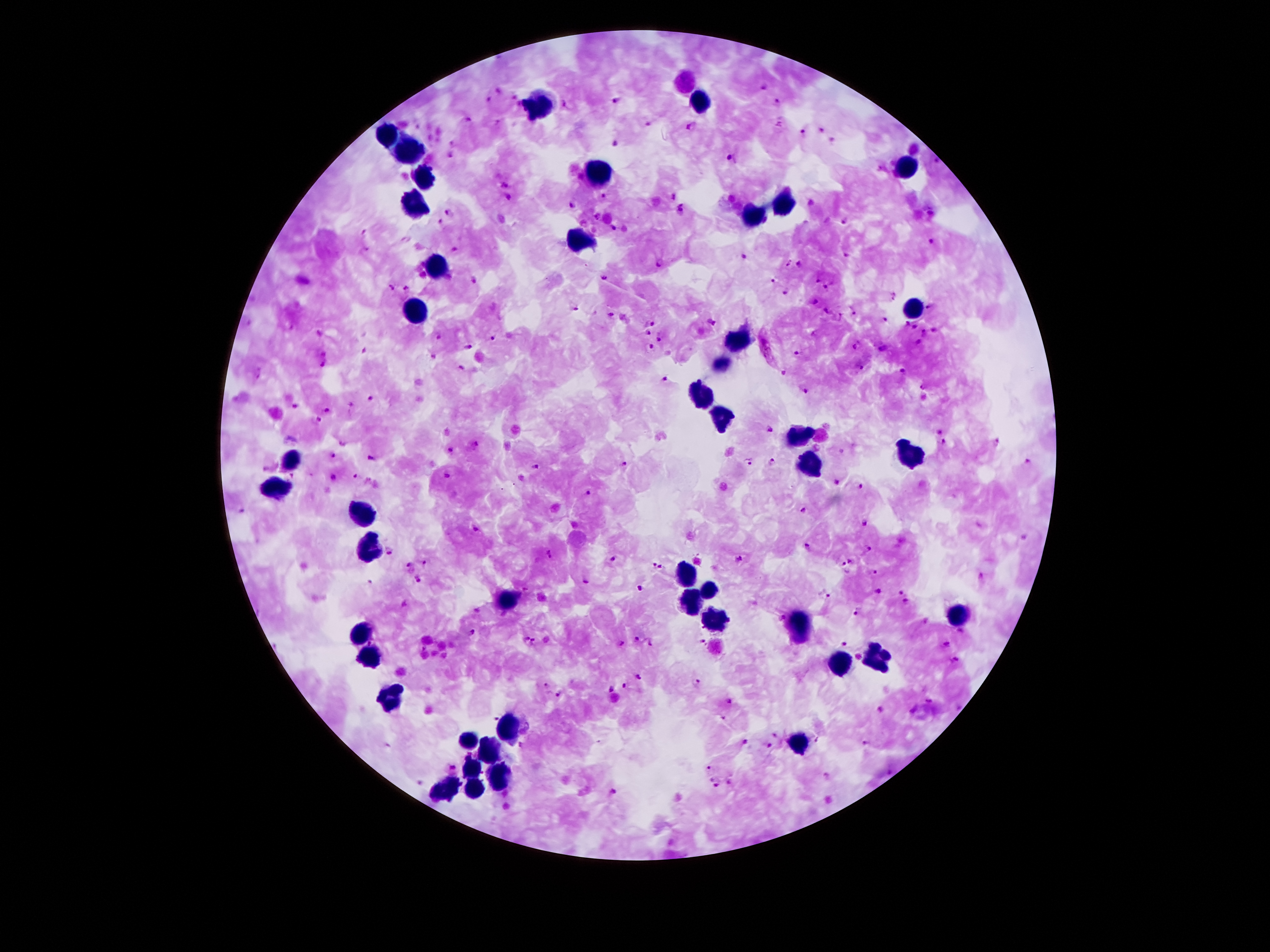 Approximate centers as {x, y} in pixels. Malaria parasite locations: {761, 87}, {499, 91}, {514, 97}, {615, 97}, {490, 99}, {778, 103}, {520, 105}, {566, 105}, {468, 120}, {496, 123}, {646, 125}, {416, 126}, {692, 128}, {822, 131}, {802, 134}, {832, 140}, {613, 142}, {453, 143}, {451, 156}, {733, 160}, {934, 161}, {579, 178}, {504, 181}, {604, 196}, {672, 197}, {509, 198}, {572, 207}, {682, 210}, {450, 211}, {930, 212}, {596, 217}, {846, 220}, {440, 222}, {615, 228}, {364, 232}, {931, 241}, {454, 248}, {366, 250}, {744, 255}, {847, 255}, {788, 261}, {662, 263}, {800, 264}, {605, 278}, {773, 280}, {473, 281}, {818, 281}, {405, 287}, {828, 288}, {391, 289}, {785, 293}, {892, 297}, {815, 301}, {930, 307}, {575, 308}, {853, 310}, {827, 312}, {610, 314}, {624, 317}, {839, 318}, {650, 321}, {711, 321}, {885, 321}, {250, 323}, {906, 323}, {914, 327}, {319, 332}, {934, 332}, {645, 333}, {925, 333}, {438, 336}, {660, 336}, {493, 337}, {918, 343}, {857, 346}, {469, 347}, {650, 347}, {765, 349}, {883, 349}, {364, 351}, {799, 352}, {325, 353}, {433, 354}, {324, 364}, {457, 367}, {860, 368}, {902, 371}, {259, 373}, {785, 373}, {665, 382}, {924, 387}, {806, 390}, {371, 398}, {295, 405}, {352, 407}, {328, 410}, {319, 421}, {770, 429}, {940, 431}, {997, 441}, {944, 444}, {343, 445}, {478, 446}, {450, 451}, {334, 455}, {370, 458}, {748, 462}, {1027, 462}, {774, 463}, {624, 464}, {534, 466}, {271, 467}, {446, 475}, {293, 476}, {334, 476}, {355, 476}, {836, 482}, {862, 486}, {588, 492}, {241, 510}, {805, 510}, {864, 522}, {475, 530}, {808, 548}, {869, 549}, {390, 550}, {548, 553}, {614, 558}, {737, 558}, {851, 561}, {424, 563}, {656, 566}, {409, 568}, {844, 569}, {874, 573}, {979, 576}, {418, 578}, {585, 581}, {371, 583}, {642, 588}, {878, 590}, {900, 591}, {824, 595}, {405, 603}, {906, 603}, {477, 610}, {857, 611}, {926, 622}, {472, 631}, {961, 631}, {524, 638}, {636, 638}, {702, 641}, {532, 643}, {620, 643}, {843, 643}, {948, 643}, {650, 644}, {422, 648}, {859, 657}, {953, 661}, {639, 676}, {696, 682}, {547, 684}, {625, 686}, {611, 689}, {559, 695}, {728, 701}, {929, 701}, {880, 709}, {913, 709}, {494, 716}, {723, 719}, {529, 730}, {776, 734}, {819, 740}, {745, 742}, {865, 743}, {769, 745}, {521, 747}, {712, 766}, {452, 769}, {827, 775}, {712, 778}, {728, 782}, {419, 783}, {718, 785}, {614, 791}. Leukocyte locations: {702, 103}, {537, 107}, {388, 136}, {409, 150}, {908, 168}, {596, 170}, {426, 179}, {786, 202}, {416, 208}, {750, 216}, {582, 242}, {436, 266}, {911, 307}, {417, 312}, {731, 342}, {722, 364}, {700, 396}, {721, 416}, {800, 436}, {911, 452}, {289, 460}, {810, 463}, {275, 490}, {357, 515}, {368, 543}, {686, 579}, {709, 590}, {688, 601}, {508, 603}, {956, 616}, {716, 622}, {800, 628}, {361, 635}, {371, 656}, {878, 656}, {841, 666}, {392, 699}, {508, 728}, {467, 741}, {800, 745}, {491, 750}, {470, 771}, {498, 777}, {474, 787}, {443, 789}. Smartphone photograph taken through the microscope eyepiece. Giemsa stain. Patient malaria status: infected with Plasmodium falciparum. Single field of view. Thick peripheral-blood smear. 100x magnification. Image is 1270×952 pixels.